Identify the blood parasite species.
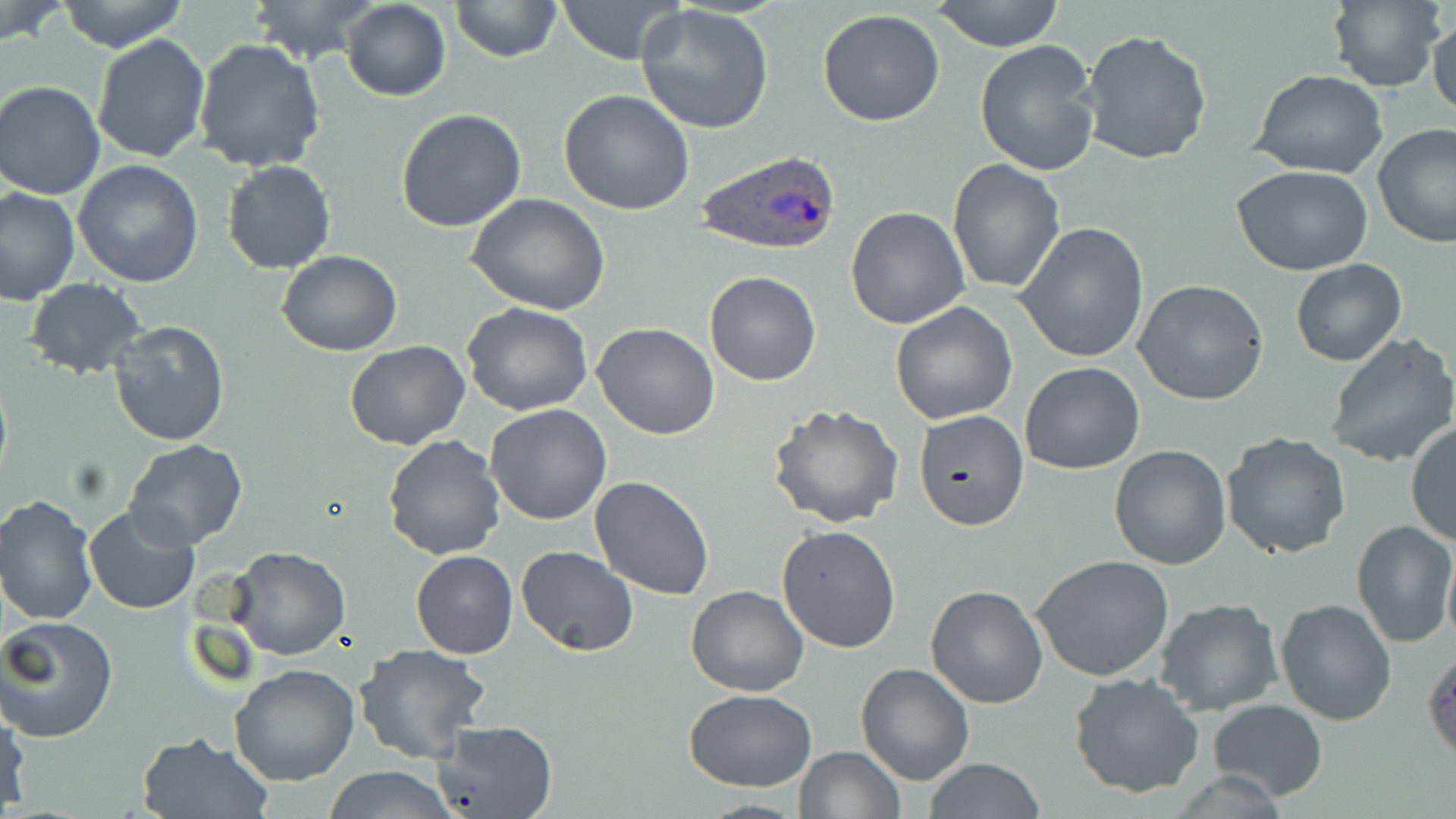
Plasmodium ovale.

Summary:
  - Coordinate format: approximate bounding boxes as [x1, y1, x2, y2] in pixels
  - Plasmodium ovale-infected red blood cell locations: [695, 148, 839, 260]
  - Uninfected red blood cell locations: [57, 0, 191, 52], [249, 0, 376, 63], [340, 0, 452, 101], [450, 0, 560, 64], [556, 0, 691, 65], [930, 0, 1067, 51], [1328, 0, 1445, 92], [1, 2, 69, 47], [633, 3, 776, 135], [1427, 8, 1456, 122], [818, 10, 946, 127], [1079, 28, 1213, 165], [91, 33, 211, 163], [975, 38, 1105, 176], [193, 39, 327, 175], [1251, 69, 1387, 180], [0, 81, 106, 200], [556, 89, 697, 214], [395, 107, 527, 232], [1371, 122, 1456, 249], [947, 158, 1066, 295], [73, 159, 203, 286], [220, 159, 337, 275], [1231, 166, 1373, 276], [0, 186, 80, 306], [466, 195, 612, 315], [844, 205, 971, 330], [1015, 222, 1151, 362], [278, 251, 402, 357], [1290, 259, 1407, 367], [702, 272, 822, 387], [22, 278, 149, 378], [1133, 278, 1272, 407], [463, 303, 595, 418], [890, 303, 1016, 424], [109, 320, 230, 447], [591, 322, 722, 439], [1326, 332, 1456, 468], [345, 342, 471, 450], [1019, 361, 1145, 474], [485, 403, 612, 525], [767, 404, 904, 529], [915, 410, 1028, 530], [1405, 422, 1456, 547], [1221, 431, 1351, 560], [382, 433, 505, 559], [124, 440, 248, 550], [1108, 445, 1232, 569], [587, 476, 715, 602], [0, 492, 99, 626], [82, 505, 199, 615], [1351, 520, 1456, 648], [776, 524, 901, 653], [514, 546, 638, 656], [1443, 546, 1456, 649], [227, 547, 351, 661], [411, 550, 520, 659], [1032, 556, 1175, 683], [925, 584, 1049, 709], [685, 585, 810, 697], [1275, 597, 1398, 724], [1154, 598, 1284, 717], [0, 614, 119, 742], [354, 643, 492, 763], [229, 664, 361, 786], [856, 664, 973, 785], [1069, 670, 1205, 797], [683, 689, 816, 791], [1206, 700, 1328, 801], [0, 702, 29, 812], [434, 719, 560, 818], [136, 731, 273, 818], [792, 746, 905, 819], [924, 757, 1045, 819], [318, 765, 460, 819]
  - Stain: May-Grünwald-Giemsa
  - Magnification: 1000x
  - Modality: optical microscopy
  - Image size: 1456×819 pixels
  - Field of view: single
  - Preparation: thin blood film